Assess the morphology of the erythrocytes.
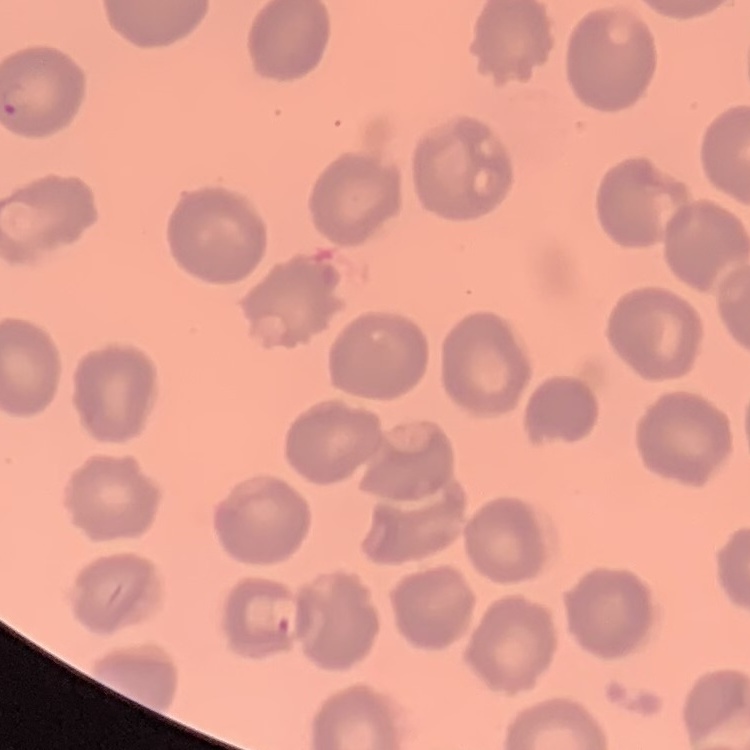
No rouleaux formation.

One tile cut from a larger photomicrograph. Stained with either Field's or Giemsa. Thin peripheral smear.